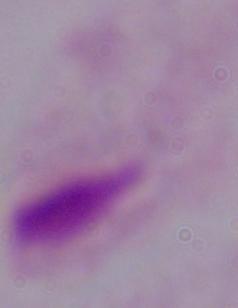
magnification = 1000x
identification = trichomonad
modality = micrograph